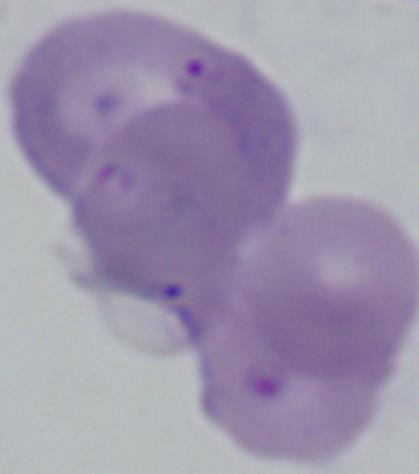
Captured at 1000x magnification. A Babesia parasite is shown. Photomicrograph.